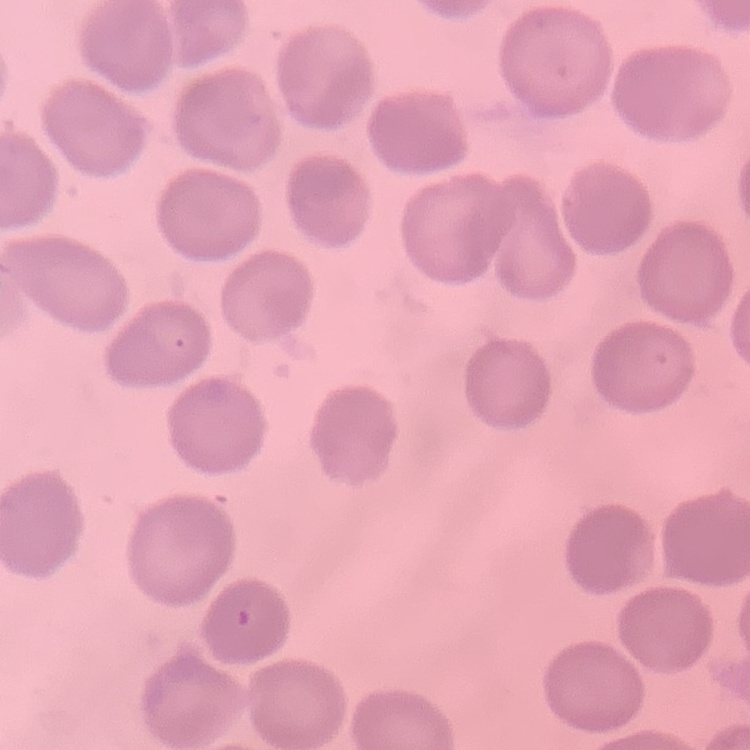
Summary:
  - Erythrocyte morphology: no rouleaux formation
  - Image type: one tile cut from a larger photomicrograph
  - Preparation: thin blood film
  - Stain: Field's or Giemsa